Evaluate for parasitized red blood cells.
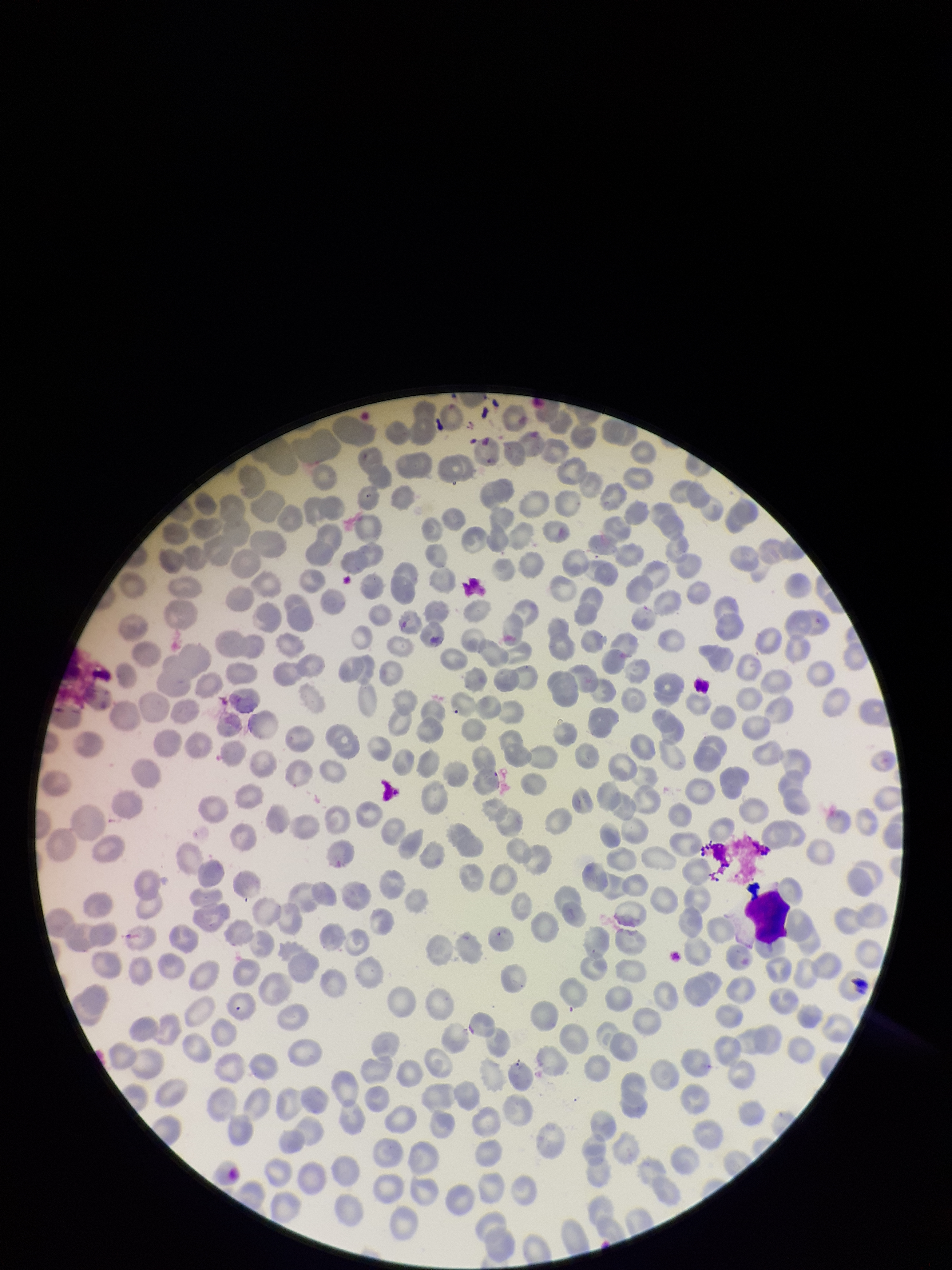

None seen.

parasitized red blood cell count = 0
stain = Giemsa
preparation = thin
image size = 952×1270 pixels
red blood cell count = 296
patient malaria status = negative
field of view = one from this slide
capture = smartphone photograph through the microscope eyepiece